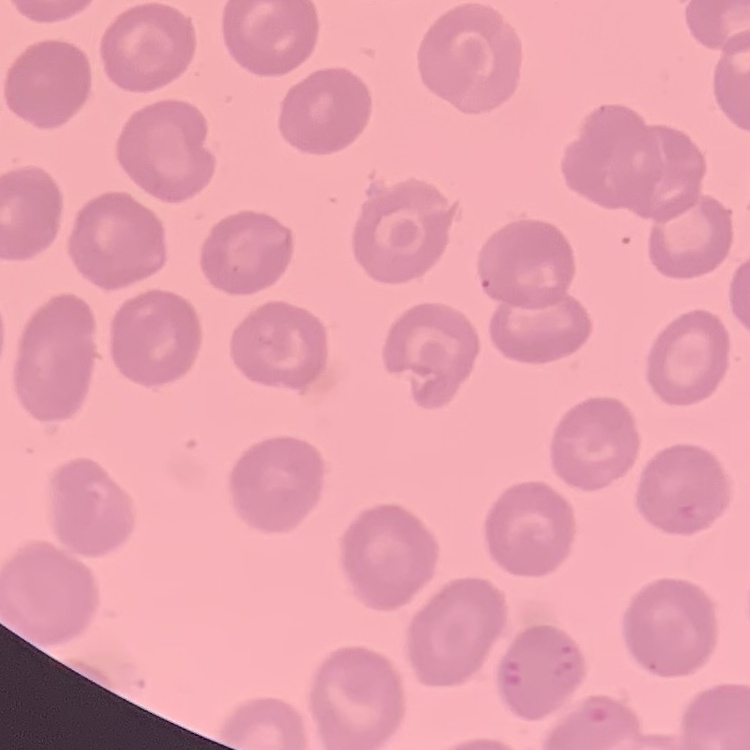
The red blood cells exhibit no rouleaux formation. Thin peripheral smear. One tile cut from a larger photomicrograph. Field's or Giemsa stain.